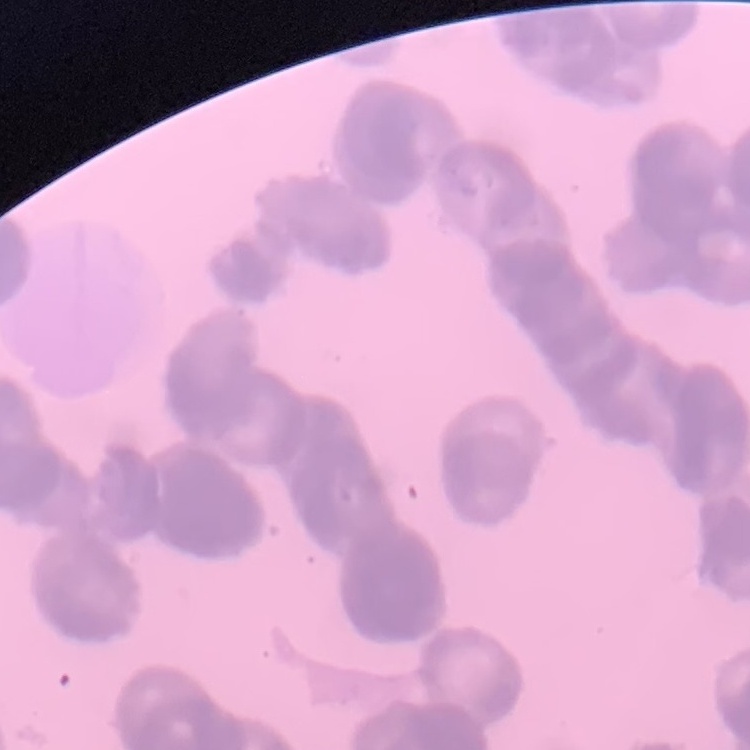

Summary:
  - Erythrocyte morphology: rouleaux formation
  - Stain: Field's or Giemsa
  - Preparation: thin blood smear
  - Image type: square crop of a larger photomicrograph